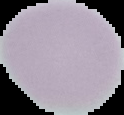
malaria status = uninfected
preparation = thin blood smear
image size = 124×115 pixels
image type = segmented cell region with the area outside set to black